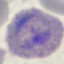

result: malaria parasites detected
capture: smartphone through the microscope eyepiece
preparation: thin smear
stain: Giemsa
image_type: cell patch, automatically extracted from a larger field of view and resized to 64 × 64 pixels